Classify this cell by malaria status.
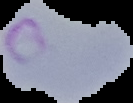
It is parasitized.

Summary:
  - Image type: segmented cell region with the area outside set to black
  - Image size: 133×103 pixels
  - Preparation: thin blood film